Outline each blood parasite and name the species.
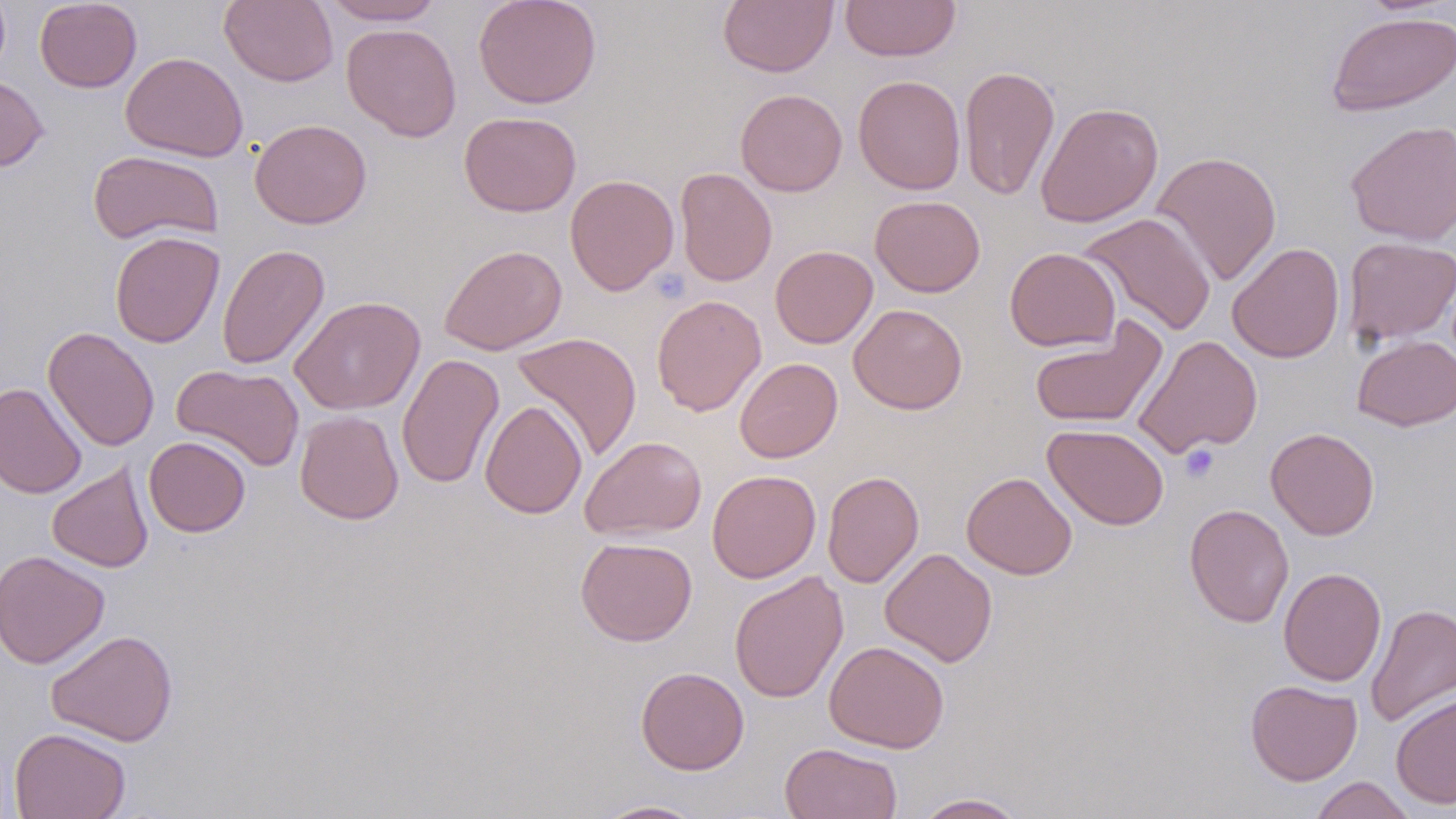

No blood parasites observed.

slide_level_diagnosis: negative for blood parasites
image_size: 1456×819 pixels
preparation: thin blood film
modality: optical microscopy
magnification: 1000x
stain: May-Grünwald-Giemsa
field_of_view: single
platelet_locations: 'approximate bounding boxes as named x1/y1/x2/y2 corners in pixels: (x1=651, y1=267, x2=690, y2=303), (x1=1179, y1=444, x2=1219, y2=483)'
uninfected_red_blood_cell_locations: 'approximate bounding boxes as named x1/y1/x2/y2 corners in pixels: (x1=35, y1=0, x2=142, y2=93), (x1=219, y1=0, x2=339, y2=87), (x1=321, y1=0, x2=445, y2=25), (x1=473, y1=0, x2=602, y2=109), (x1=718, y1=0, x2=837, y2=77), (x1=841, y1=0, x2=960, y2=61), (x1=1325, y1=12, x2=1456, y2=117), (x1=341, y1=23, x2=461, y2=141), (x1=121, y1=52, x2=248, y2=162), (x1=959, y1=66, x2=1060, y2=201), (x1=0, y1=73, x2=49, y2=173), (x1=853, y1=75, x2=966, y2=195), (x1=735, y1=88, x2=847, y2=197), (x1=1035, y1=101, x2=1164, y2=228), (x1=458, y1=111, x2=582, y2=217), (x1=249, y1=118, x2=372, y2=229), (x1=1344, y1=119, x2=1456, y2=246), (x1=88, y1=150, x2=224, y2=246), (x1=1151, y1=150, x2=1283, y2=286), (x1=675, y1=167, x2=777, y2=287), (x1=565, y1=174, x2=679, y2=296), (x1=870, y1=195, x2=985, y2=296), (x1=1077, y1=212, x2=1217, y2=337), (x1=109, y1=231, x2=224, y2=348), (x1=1342, y1=236, x2=1456, y2=346), (x1=1227, y1=242, x2=1345, y2=363), (x1=217, y1=243, x2=330, y2=370), (x1=439, y1=244, x2=567, y2=355), (x1=770, y1=245, x2=878, y2=348), (x1=1004, y1=247, x2=1121, y2=352), (x1=651, y1=294, x2=766, y2=416), (x1=289, y1=296, x2=426, y2=415), (x1=849, y1=304, x2=967, y2=414), (x1=1028, y1=320, x2=1167, y2=430), (x1=43, y1=326, x2=160, y2=451), (x1=511, y1=332, x2=643, y2=462), (x1=1133, y1=334, x2=1263, y2=458), (x1=1352, y1=335, x2=1456, y2=431), (x1=396, y1=352, x2=504, y2=489), (x1=734, y1=358, x2=842, y2=463), (x1=172, y1=363, x2=305, y2=472), (x1=0, y1=382, x2=87, y2=499), (x1=480, y1=400, x2=587, y2=519), (x1=295, y1=410, x2=404, y2=524), (x1=1043, y1=424, x2=1170, y2=530), (x1=1265, y1=427, x2=1380, y2=540), (x1=579, y1=435, x2=707, y2=540), (x1=144, y1=436, x2=250, y2=537), (x1=47, y1=462, x2=154, y2=572), (x1=706, y1=469, x2=821, y2=583), (x1=823, y1=470, x2=924, y2=588), (x1=961, y1=471, x2=1077, y2=580), (x1=1184, y1=503, x2=1294, y2=628), (x1=575, y1=536, x2=698, y2=646), (x1=880, y1=548, x2=997, y2=667), (x1=0, y1=550, x2=109, y2=668), (x1=1278, y1=567, x2=1386, y2=686), (x1=729, y1=570, x2=849, y2=704), (x1=1365, y1=603, x2=1456, y2=728), (x1=46, y1=629, x2=178, y2=747), (x1=824, y1=640, x2=949, y2=753), (x1=635, y1=666, x2=749, y2=774), (x1=1245, y1=680, x2=1362, y2=785), (x1=1390, y1=692, x2=1456, y2=809), (x1=9, y1=727, x2=131, y2=819), (x1=779, y1=742, x2=903, y2=819), (x1=1309, y1=776, x2=1417, y2=819), (x1=912, y1=793, x2=1027, y2=818), (x1=592, y1=799, x2=710, y2=818)'